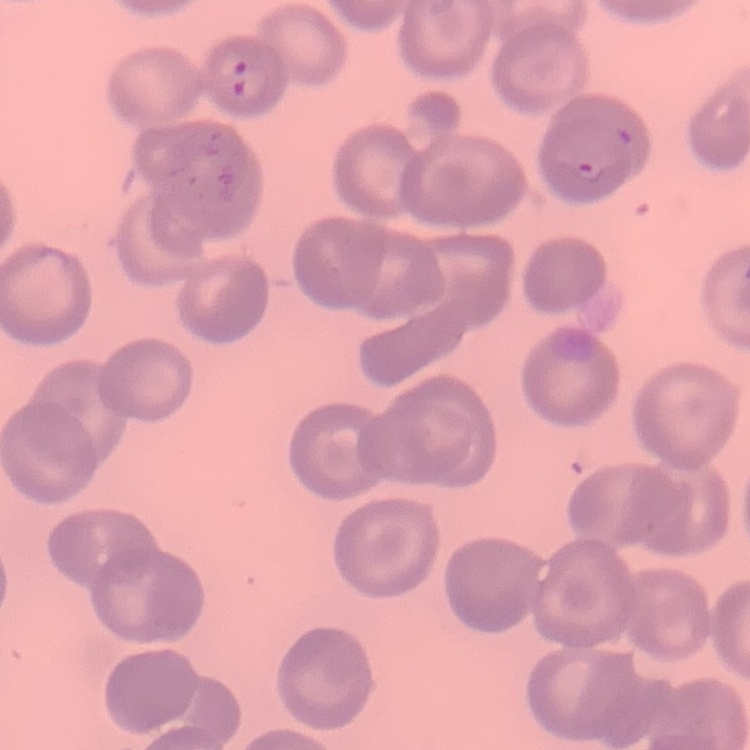

The erythrocytes exhibit no rouleaux formation. Thin peripheral smear. Stained with either Field's or Giemsa. Square crop of a larger photomicrograph.